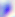
Summary:
  - Modality: photomicrograph
  - Identification: Toxoplasma gondii
  - Magnification: 400x